Report the malaria status of this cell.
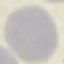
Uninfected.

image type = cell patch, automatically extracted from a larger field of view and resized to 64 × 64 pixels
stain = Giemsa
capture = smartphone through the microscope eyepiece
preparation = thin blood smear